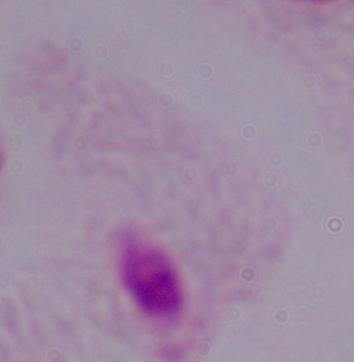

Summary:
  - Modality: photomicrograph
  - Magnification: 1000x
  - Identification: trichomonad